Locate every Plasmodium falciparum-infected red blood cell.
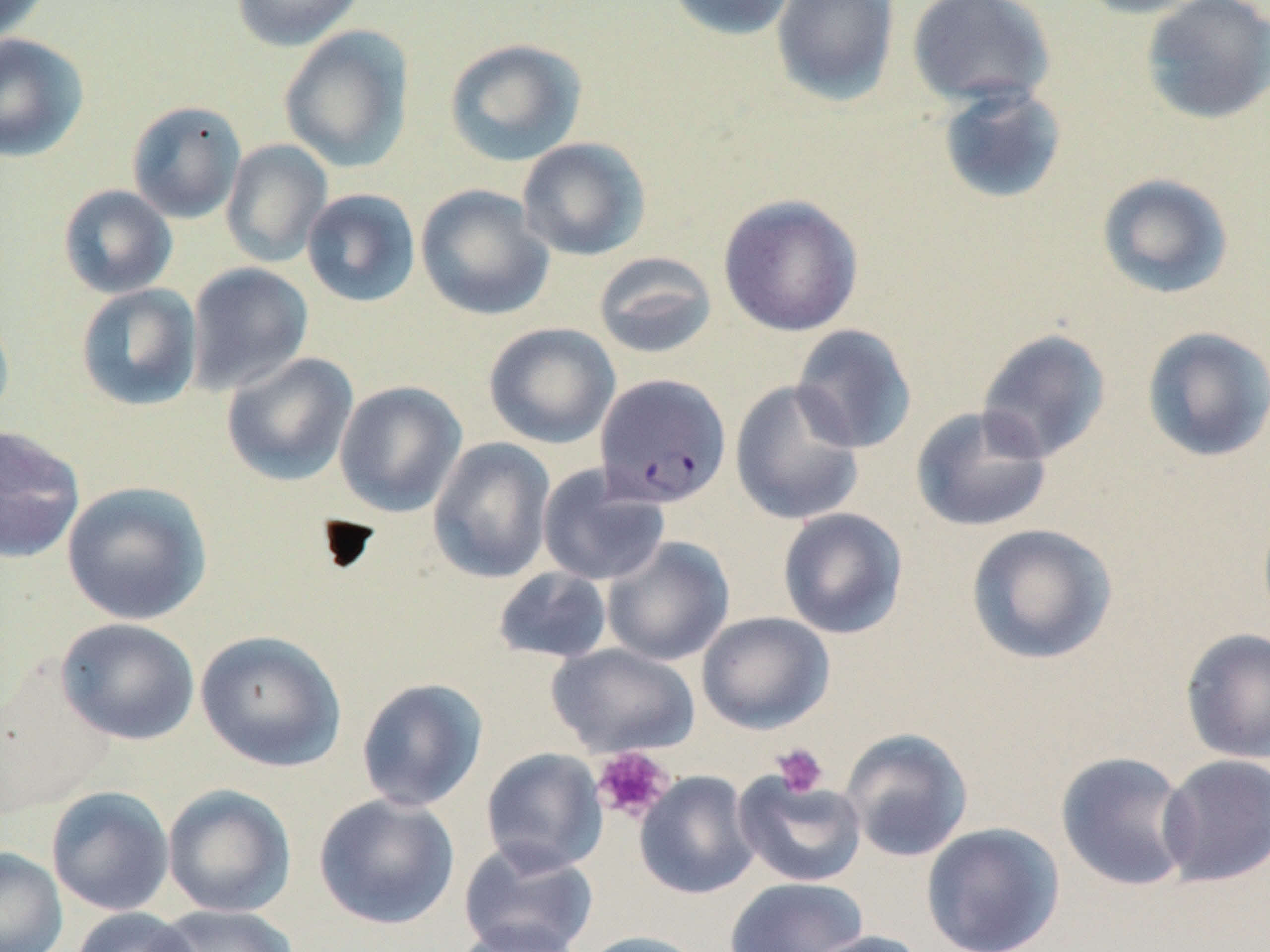
Approximate bounding boxes as named x1/y1/x2/y2 corners in pixels.
Plasmodium falciparum-infected red blood cells: (x1=595, y1=373, x2=732, y2=509).

{
  "slide_level_diagnosis": "Plasmodium falciparum",
  "uninfected_red_blood_cell_locations": "approximate bounding boxes as named x1/y1/x2/y2 corners in pixels: (x1=0, y1=0, x2=52, y2=43), (x1=232, y1=0, x2=365, y2=51), (x1=666, y1=0, x2=799, y2=41), (x1=770, y1=0, x2=901, y2=108), (x1=1072, y1=0, x2=1215, y2=19), (x1=1139, y1=0, x2=1270, y2=125), (x1=906, y1=1, x2=1056, y2=109), (x1=278, y1=25, x2=415, y2=173), (x1=0, y1=33, x2=89, y2=162), (x1=443, y1=38, x2=587, y2=167), (x1=936, y1=84, x2=1068, y2=205), (x1=126, y1=100, x2=247, y2=224), (x1=517, y1=137, x2=651, y2=261), (x1=221, y1=139, x2=333, y2=267), (x1=1097, y1=173, x2=1234, y2=300), (x1=58, y1=184, x2=178, y2=299), (x1=415, y1=184, x2=554, y2=321), (x1=301, y1=188, x2=421, y2=308), (x1=716, y1=193, x2=864, y2=337), (x1=593, y1=251, x2=718, y2=359), (x1=186, y1=262, x2=314, y2=396), (x1=75, y1=283, x2=203, y2=412), (x1=0, y1=304, x2=15, y2=427), (x1=483, y1=322, x2=620, y2=449), (x1=791, y1=324, x2=917, y2=454), (x1=1141, y1=326, x2=1270, y2=463), (x1=976, y1=328, x2=1112, y2=463), (x1=221, y1=352, x2=359, y2=486), (x1=334, y1=380, x2=467, y2=517), (x1=729, y1=380, x2=865, y2=526), (x1=910, y1=405, x2=1053, y2=533), (x1=0, y1=425, x2=86, y2=564), (x1=428, y1=438, x2=556, y2=584), (x1=537, y1=465, x2=672, y2=586), (x1=61, y1=481, x2=213, y2=625), (x1=777, y1=507, x2=908, y2=640), (x1=965, y1=523, x2=1118, y2=665), (x1=602, y1=536, x2=735, y2=667), (x1=491, y1=566, x2=614, y2=665), (x1=697, y1=611, x2=834, y2=734), (x1=55, y1=617, x2=200, y2=745), (x1=1180, y1=627, x2=1270, y2=764), (x1=195, y1=630, x2=349, y2=772), (x1=546, y1=643, x2=701, y2=758), (x1=356, y1=677, x2=488, y2=812), (x1=840, y1=728, x2=974, y2=862), (x1=481, y1=747, x2=608, y2=874), (x1=1055, y1=750, x2=1195, y2=892), (x1=1157, y1=754, x2=1270, y2=888), (x1=634, y1=770, x2=760, y2=900), (x1=733, y1=771, x2=868, y2=888), (x1=162, y1=784, x2=296, y2=918), (x1=46, y1=785, x2=174, y2=916), (x1=313, y1=793, x2=460, y2=930), (x1=920, y1=822, x2=1065, y2=952), (x1=457, y1=839, x2=599, y2=952), (x1=0, y1=846, x2=67, y2=952), (x1=724, y1=876, x2=869, y2=952), (x1=152, y1=904, x2=299, y2=952), (x1=69, y1=909, x2=201, y2=952), (x1=451, y1=921, x2=586, y2=952), (x1=573, y1=930, x2=711, y2=952), (x1=796, y1=930, x2=932, y2=952)",
  "platelet_locations": "approximate bounding boxes as named x1/y1/x2/y2 corners in pixels: (x1=771, y1=742, x2=829, y2=798), (x1=592, y1=747, x2=675, y2=823)",
  "preparation": "thin blood smear",
  "image_size": "1270×952 pixels",
  "magnification": "1000x",
  "modality": "optical microscopy",
  "stain": "May-Grünwald-Giemsa",
  "field_of_view": "one of a larger specimen"
}